Identify the parasite.
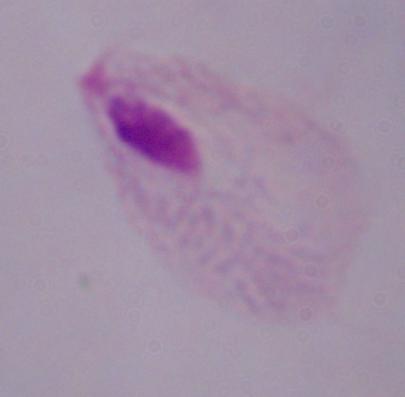

A trichomonad.

Photomicrograph. 1000x magnification.